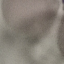

malaria status = uninfected
stain = Giemsa
image type = cell patch, automatically extracted from a larger field of view and resized to 64 × 64 pixels
preparation = thin blood smear
capture = smartphone through the microscope eyepiece